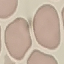

Result: negative for malaria parasites. Acquired by smartphone through the microscope eyepiece. Thin blood smear. Cell patch, automatically extracted from a larger field of view and resized to 64 × 64 pixels. Giemsa stain.